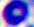

magnification: 400x
identification: white blood cell
modality: photomicrograph